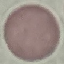

Summary:
  - Malaria status: uninfected
  - Preparation: thin blood smear
  - Image type: automatically extracted cell patch, resized to 64 × 64 pixels
  - Stain: Giemsa
  - Capture: smartphone through the microscope eyepiece